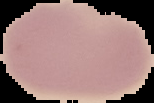

Summary:
  - Image type: segmented cell region with the area outside set to black
  - Result: negative for Plasmodium parasites
  - Image size: 154×103 pixels
  - Preparation: thin blood film